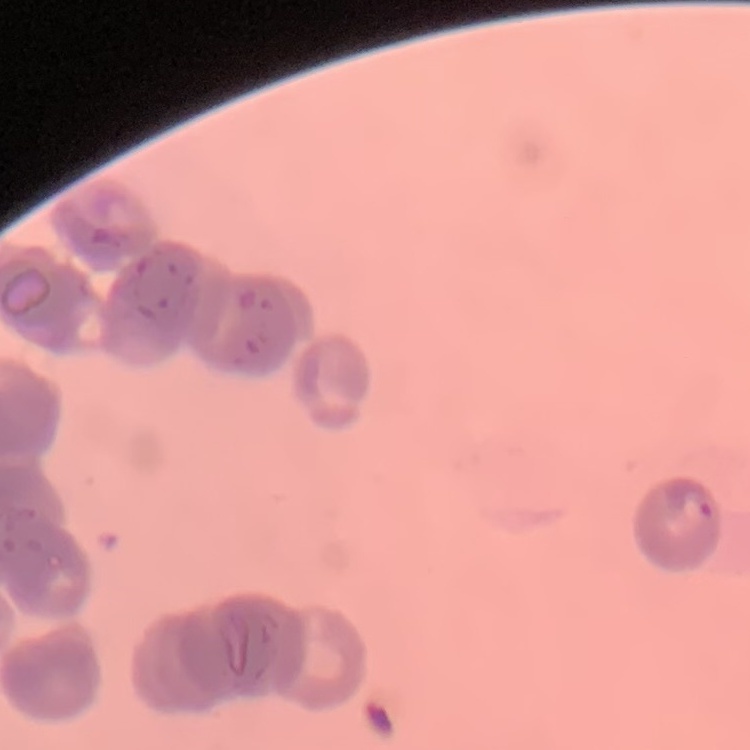
erythrocyte morphology = rouleaux formation
preparation = thin blood smear
stain = Field's or Giemsa
image type = one tile cut from a larger photomicrograph